Give the position of every Plasmodium parasite.
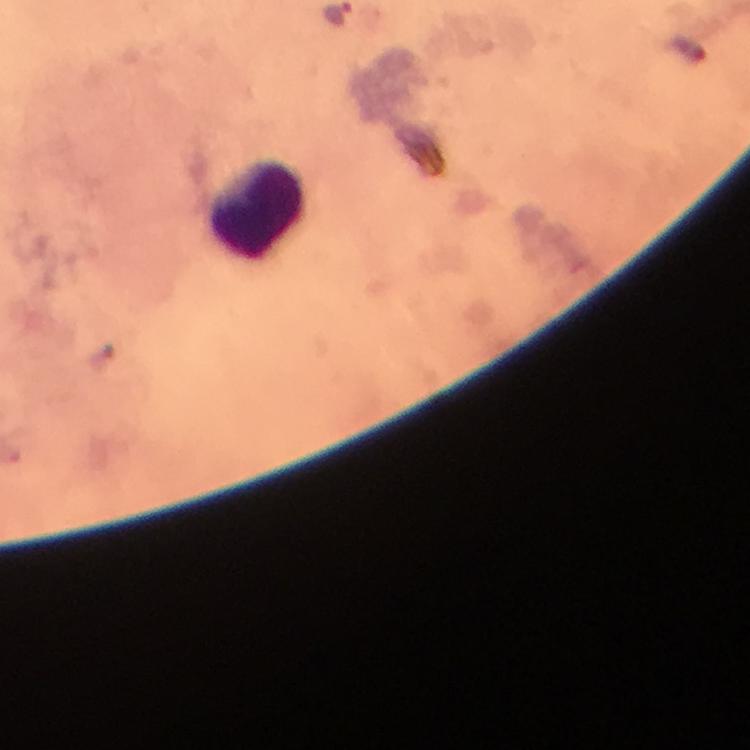

No Plasmodium parasites detected.

{
  "capture": "smartphone photograph through a microscope",
  "cropped_from": "one field of view",
  "immersion_oil": "used",
  "image_size": "750×750 pixels",
  "stain": "Giemsa",
  "leukocyte_locations": "approximate object centers, in pixels from the top-left corner: (x=255, y=212)",
  "context": "from a malaria diagnostic workup",
  "preparation": "thick blood film",
  "magnification": "100x"
}